Identify the parasite.
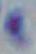
Toxoplasma gondii.

Summary:
  - Modality: micrograph
  - Magnification: 1000x